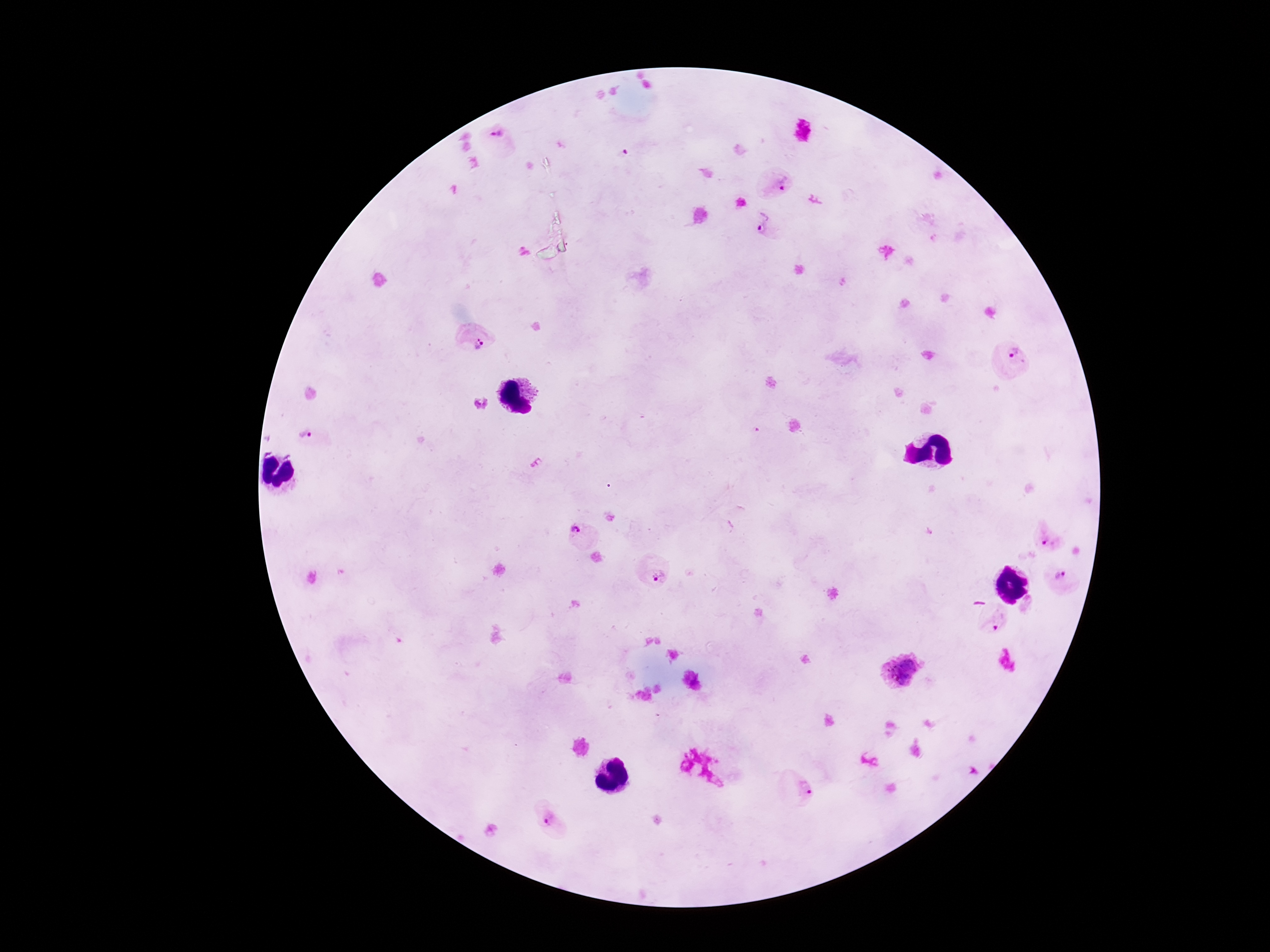
Approximate object centers, in pixels from the top-left corner.
Summary:
  - Plasmodium parasite locations: (x=497, y=140), (x=775, y=185), (x=763, y=227), (x=475, y=339), (x=1014, y=359), (x=312, y=439), (x=579, y=533), (x=1048, y=536), (x=652, y=572), (x=1062, y=582), (x=992, y=620), (x=901, y=672), (x=797, y=787), (x=552, y=820)
  - Patient malaria status: positive
  - Field of view: one from this slide
  - Stain: Giemsa
  - Magnification: 100x
  - Preparation: thick blood film
  - Image size: 1270×952 pixels
  - Capture: smartphone camera through the microscope eyepiece